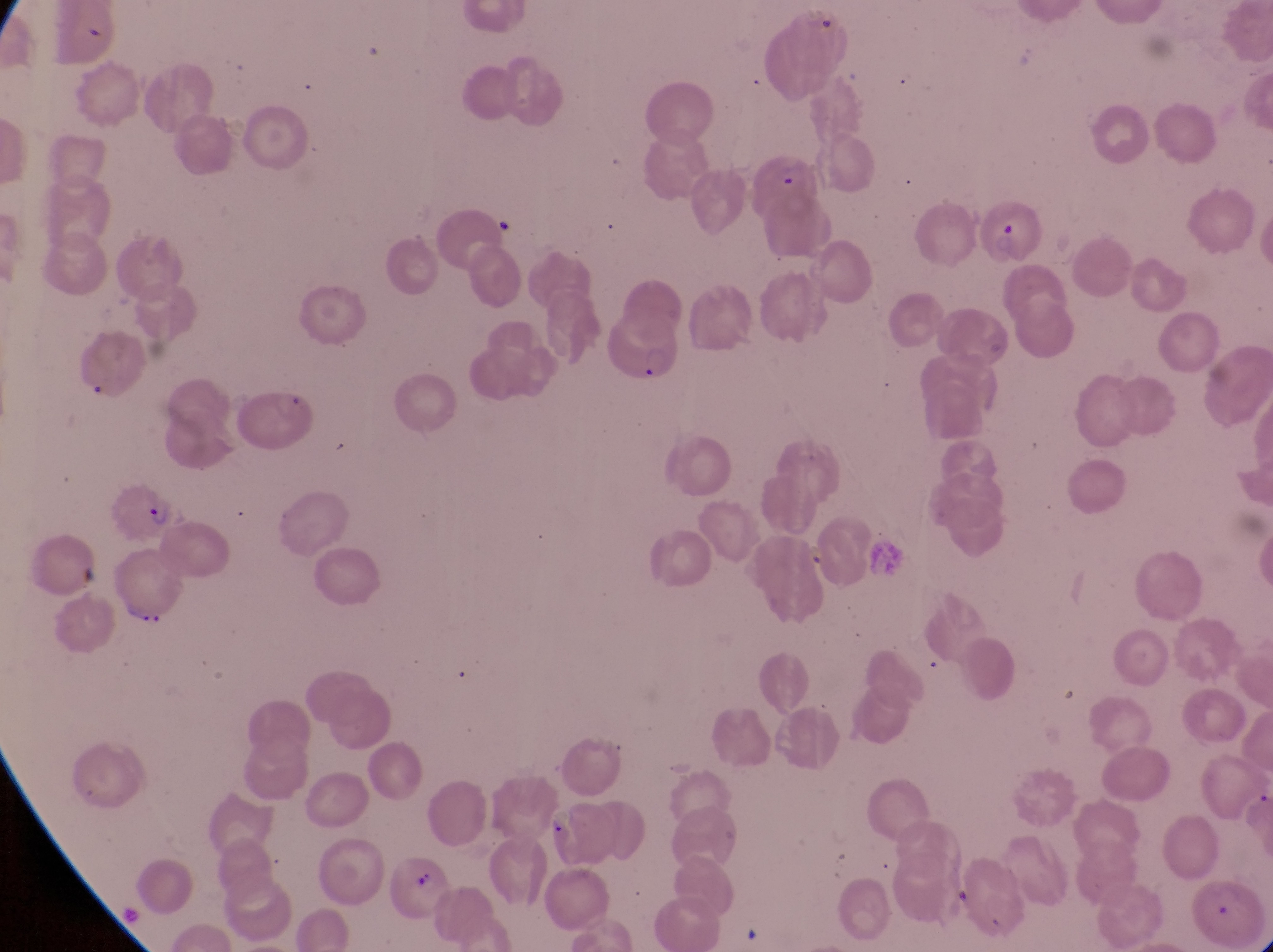
Approximate bounding boxes as left top right bottom in pixels.
Summary:
  - Trophozoite locations: 804 537 831 574; 120 597 170 637; 546 806 569 838
  - Artifact (platelet-like body, stain precipitate, or debris) locations: 74 556 104 591; 948 881 975 916
  - Parasitised red blood cell locations: 747 150 819 222; 976 200 1046 267; 604 302 689 387; 112 482 181 547; 375 846 455 920; 1195 876 1257 938
  - Country: Uganda
  - Field of view: single
  - Capture: smartphone photograph through the eyepiece of an Olympus CX-23 microscope
  - Image size: 1273×952 pixels
  - Magnification: 1000x
  - Preparation: thin blood film